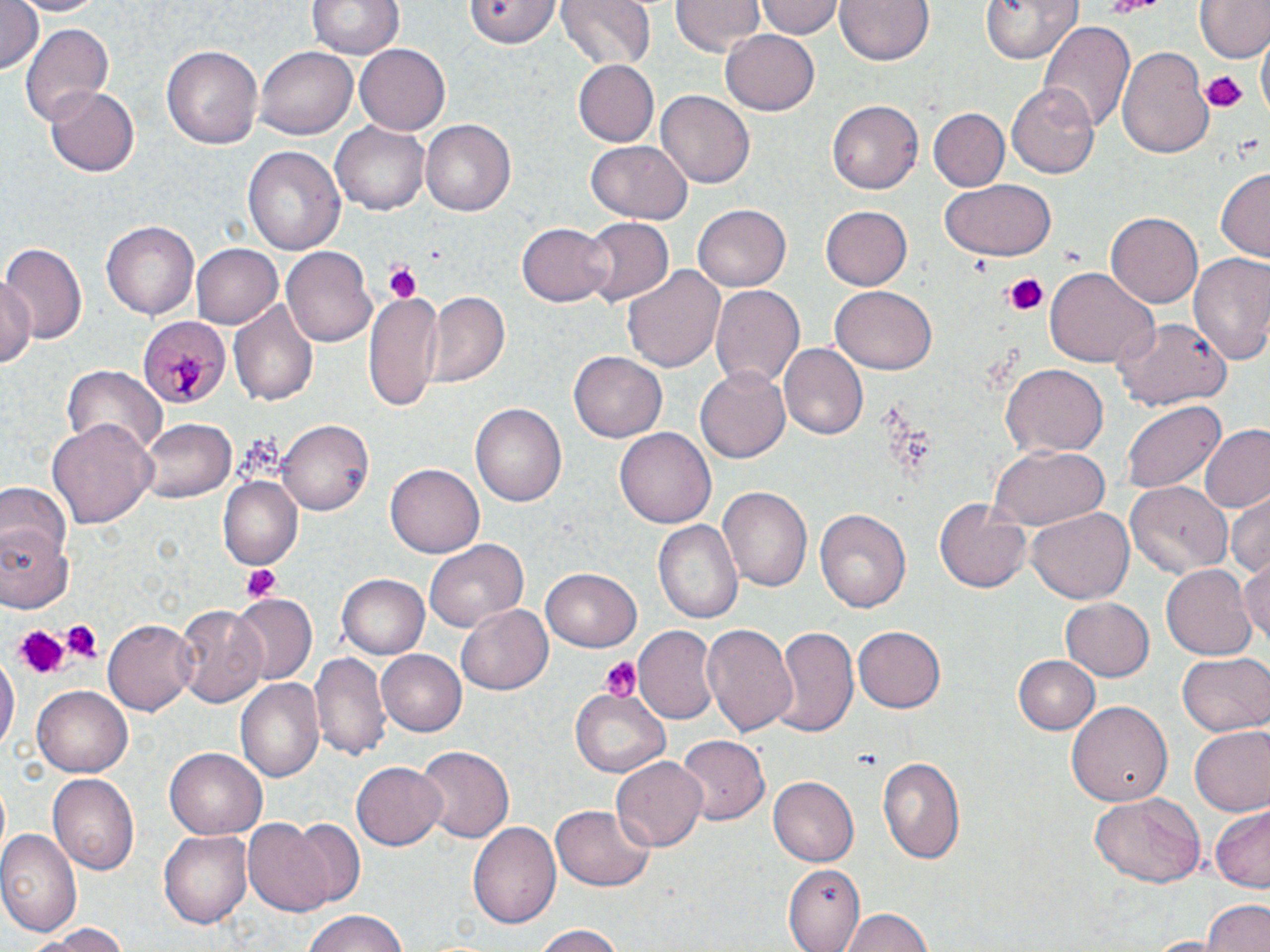

slide_level_diagnosis: Plasmodium malariae
magnification: 1000x
field_of_view: single
modality: optical microscopy
uninfected_red_blood_cell_locations: 'approximate bounding boxes as (x1, y1, x2, y2) in pixels: (0, 0, 46, 76), (9, 0, 104, 15), (308, 0, 403, 61), (462, 0, 561, 48), (556, 0, 659, 70), (672, 0, 763, 56), (756, 0, 845, 40), (834, 0, 936, 67), (980, 0, 1082, 64), (1194, 2, 1268, 62), (1039, 22, 1134, 133), (22, 23, 114, 125), (720, 29, 820, 115), (1259, 37, 1268, 119), (355, 44, 449, 136), (163, 45, 263, 150), (1117, 45, 1213, 160), (258, 46, 357, 140), (572, 60, 658, 148), (1007, 84, 1100, 178), (46, 85, 139, 176), (656, 91, 754, 188), (828, 99, 923, 194), (930, 109, 1009, 192), (331, 120, 432, 215), (420, 120, 516, 217), (586, 140, 692, 225), (242, 144, 345, 259), (1216, 168, 1269, 261), (941, 178, 1056, 261), (694, 204, 790, 291), (819, 205, 911, 290), (1106, 211, 1203, 307), (101, 217, 198, 318), (580, 218, 672, 309), (517, 222, 613, 305), (0, 243, 85, 347), (194, 243, 282, 327), (282, 246, 377, 350), (1187, 254, 1270, 367), (621, 262, 725, 371), (1044, 267, 1159, 368), (0, 275, 37, 373), (710, 284, 805, 392), (363, 288, 442, 411), (830, 288, 935, 374), (423, 292, 509, 389), (230, 301, 319, 406), (1114, 318, 1231, 409), (778, 343, 869, 440), (569, 352, 666, 442), (63, 365, 166, 456), (1003, 365, 1106, 457), (694, 366, 790, 464), (1120, 400, 1226, 494), (469, 402, 566, 510), (48, 417, 156, 532), (138, 419, 235, 503), (278, 420, 372, 516), (1199, 426, 1270, 516), (615, 427, 716, 529), (989, 445, 1111, 529), (388, 463, 485, 556), (217, 476, 304, 569), (1126, 479, 1233, 577), (0, 480, 69, 559), (719, 486, 812, 593), (1225, 493, 1269, 579), (935, 496, 1034, 592), (814, 507, 911, 613), (1028, 508, 1134, 604), (654, 519, 742, 624), (0, 528, 73, 613), (423, 538, 528, 632), (1238, 557, 1270, 652), (1162, 564, 1257, 661), (542, 568, 641, 652), (338, 575, 430, 659), (231, 595, 317, 686), (1060, 597, 1155, 681), (457, 604, 553, 693), (175, 605, 268, 708), (105, 619, 197, 714), (702, 623, 800, 739), (634, 625, 720, 726), (772, 626, 859, 737), (854, 627, 945, 714), (376, 649, 466, 736), (312, 651, 389, 760), (0, 653, 18, 757), (1178, 653, 1270, 738), (1012, 654, 1100, 734), (235, 676, 324, 785), (33, 687, 134, 776), (571, 689, 672, 777), (1067, 700, 1171, 808), (1189, 726, 1269, 816), (675, 735, 771, 825), (415, 745, 514, 845), (165, 746, 267, 836), (878, 754, 967, 862), (610, 757, 707, 852), (350, 760, 447, 849), (48, 773, 139, 874), (769, 777, 858, 866), (1089, 793, 1205, 888), (1210, 804, 1270, 892), (549, 805, 656, 891), (467, 818, 560, 927), (287, 820, 363, 905), (244, 821, 335, 918), (161, 830, 254, 930), (0, 831, 82, 939), (782, 864, 865, 951), (1203, 899, 1270, 952), (840, 905, 935, 951), (297, 911, 413, 952), (33, 923, 136, 951), (532, 925, 632, 951)'
platelet_locations: 'approximate bounding boxes as (x1, y1, x2, y2) in pixels: (1104, 0, 1164, 18), (1202, 72, 1246, 113), (382, 261, 422, 304), (1002, 274, 1047, 316), (242, 565, 281, 602), (58, 620, 102, 660), (15, 624, 65, 678), (601, 658, 640, 702)'
preparation: thin blood smear
stain: May-Grünwald-Giemsa
image_size: 1270×952 pixels
plasmodium_malariae_infected_red_blood_cell_locations: 'approximate bounding boxes as (x1, y1, x2, y2) in pixels: (136, 315, 229, 409)'